Give the position of every Plasmodium parasite visible.
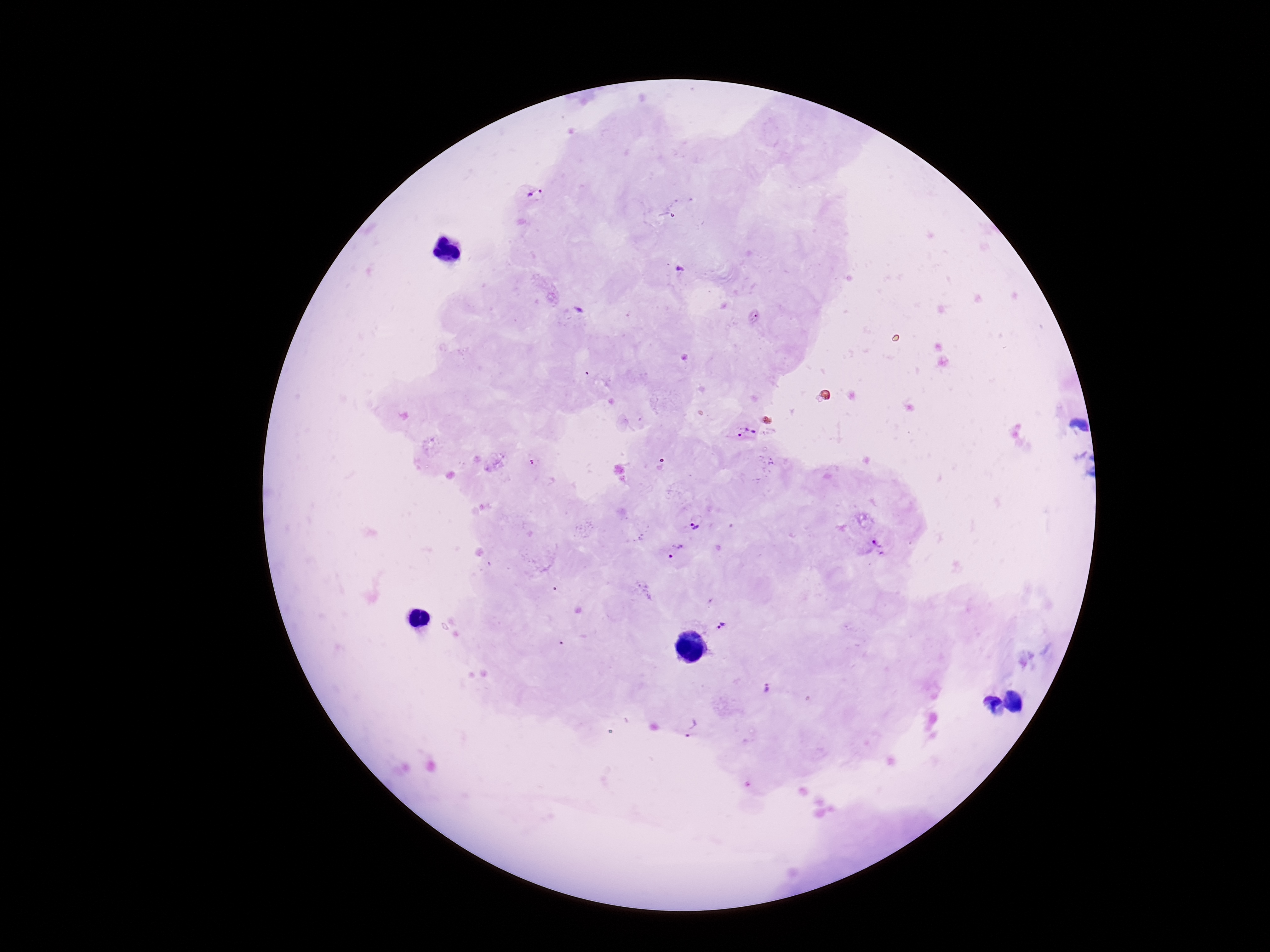

Approximate centers as (x, y) in pixels.
Plasmodium parasites: (536, 196), (679, 269), (746, 432), (771, 463), (694, 526), (678, 549), (876, 549), (724, 626), (765, 688), (694, 728).

Summary:
  - Image size: 1270×952 pixels
  - Patient malaria status: positive
  - Magnification: 100x
  - Capture: smartphone camera through the microscope eyepiece
  - Preparation: thick blood smear
  - Stain: Giemsa
  - Field of view: single